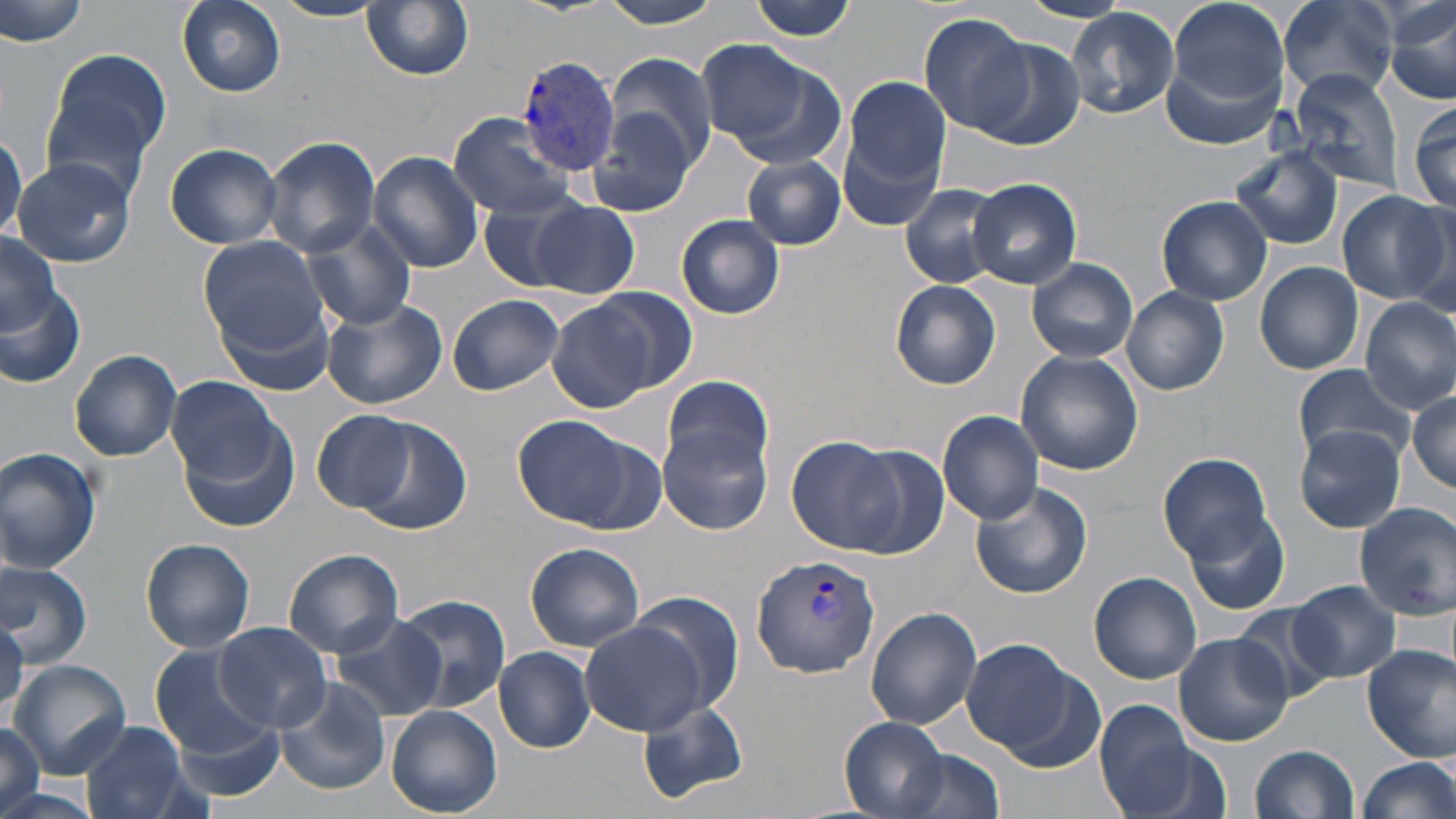

slide-level diagnosis = Plasmodium vivax
field of view = one of a larger specimen
magnification = 1000x
stain = May-Grünwald-Giemsa
preparation = thin blood smear
uninfected red blood cell locations = approximate bounding boxes as (x1,y1)-(x2,y2) corner pairs in pixels: (175,0)-(286,97), (599,0)-(728,30), (749,0)-(862,41), (1164,0)-(1289,119), (1280,0)-(1398,98), (1385,0)-(1456,107), (3,1)-(90,48), (269,1)-(389,22), (363,1)-(475,80), (1064,7)-(1179,120), (919,13)-(1031,136), (969,35)-(1086,151), (697,38)-(823,151), (39,44)-(176,199), (603,51)-(718,177), (1287,70)-(1405,191), (842,75)-(950,195), (587,88)-(708,220), (1408,100)-(1456,213), (447,112)-(579,220), (0,123)-(25,246), (261,135)-(381,257), (164,142)-(283,250), (1234,149)-(1344,249), (368,150)-(485,274), (12,156)-(138,268), (742,156)-(846,250), (968,178)-(1082,289), (898,183)-(1009,289), (1337,190)-(1452,306), (476,195)-(603,293), (1156,195)-(1272,306), (1396,196)-(1456,314), (532,199)-(639,300), (676,214)-(786,321), (301,218)-(418,330), (196,232)-(329,360), (0,234)-(70,345), (1027,258)-(1138,364), (1255,261)-(1364,375), (0,270)-(86,388), (890,281)-(1001,388), (591,287)-(698,391), (1121,287)-(1229,396), (448,294)-(566,396), (545,295)-(674,412), (1360,296)-(1456,412), (322,300)-(447,410), (70,350)-(182,461), (1016,351)-(1143,474), (1293,362)-(1415,463), (661,374)-(776,489), (166,376)-(285,484), (1409,388)-(1456,491), (313,410)-(421,514), (937,411)-(1043,526), (343,414)-(476,537), (514,414)-(641,528), (661,418)-(774,536), (1292,425)-(1408,534), (181,426)-(299,537), (789,436)-(908,553), (0,447)-(101,572), (849,447)-(948,559), (1158,451)-(1275,563), (969,480)-(1093,601), (1353,502)-(1456,619), (1185,510)-(1292,617), (141,538)-(256,653), (524,542)-(646,652), (282,548)-(403,658), (0,558)-(93,667), (1090,572)-(1202,684), (1286,581)-(1401,684), (397,595)-(508,716), (626,595)-(744,718), (1236,603)-(1339,707), (865,606)-(983,729), (0,612)-(25,712), (330,612)-(447,723), (580,619)-(713,735), (213,622)-(332,731), (1174,632)-(1291,746), (959,638)-(1087,760), (1362,645)-(1456,763), (155,647)-(273,759), (496,647)-(595,751), (8,659)-(132,778), (273,676)-(390,796), (636,697)-(748,805), (1095,701)-(1210,819), (386,706)-(502,817), (164,709)-(290,806), (841,717)-(951,816), (81,721)-(191,819), (0,722)-(46,819), (1250,744)-(1360,819), (895,745)-(1004,818), (1355,756)-(1456,819)
modality = light microscopy
Plasmodium vivax-infected red blood cell locations = approximate bounding boxes as (x1,y1)-(x2,y2) corner pairs in pixels: (515,54)-(623,173), (751,556)-(881,678)
image size = 1456×819 pixels